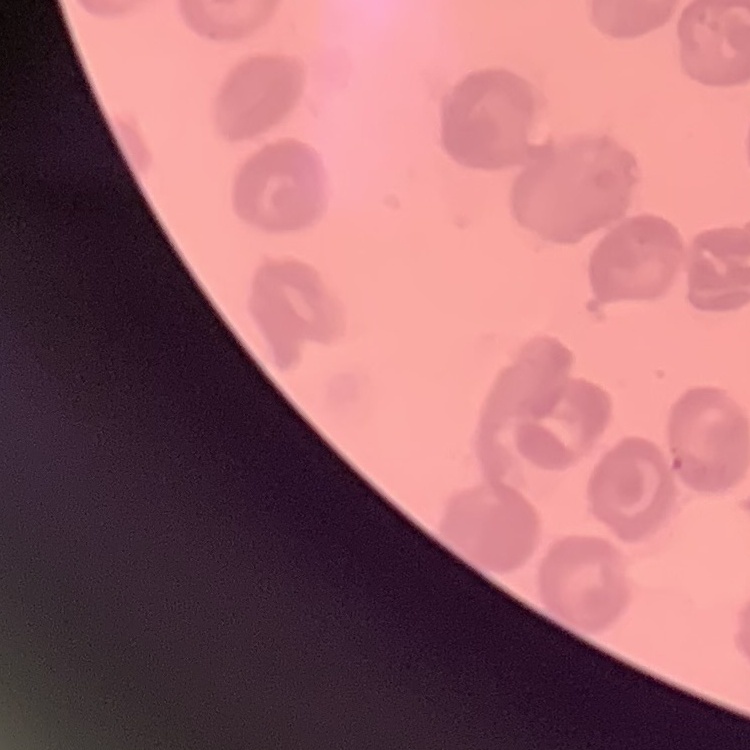 The erythrocytes show no rouleaux formation. Stained with either Field's or Giemsa. Square crop of a larger photomicrograph. Thin blood film.